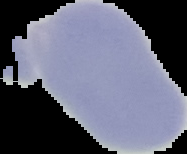
image type = segmented cell region with the area outside set to black
malaria status = uninfected
preparation = thin blood smear
image size = 187×154 pixels